Describe the morphology of the erythrocytes.
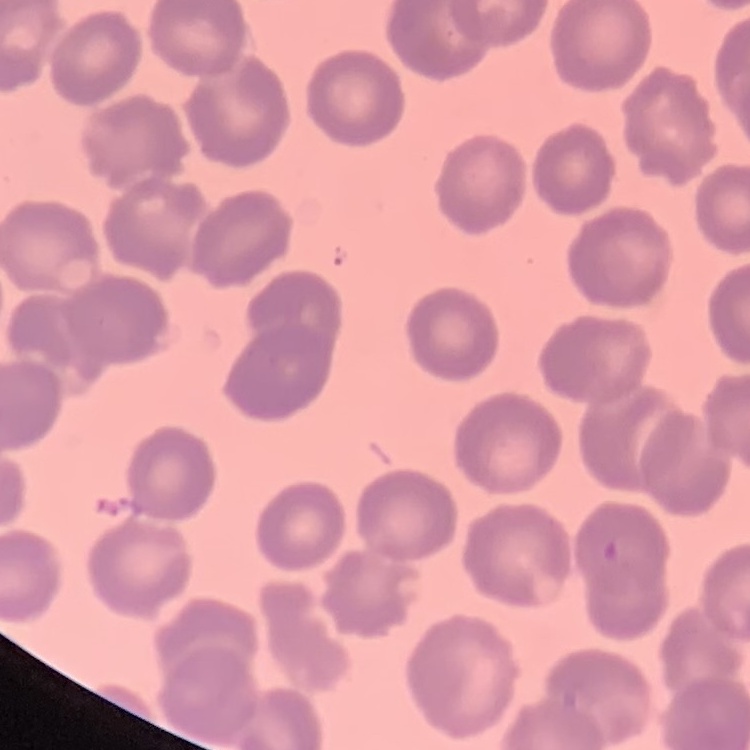

They show no rouleaux formation.

Summary:
  - Stain: Field's or Giemsa
  - Preparation: thin peripheral smear
  - Image type: square crop of a larger photomicrograph